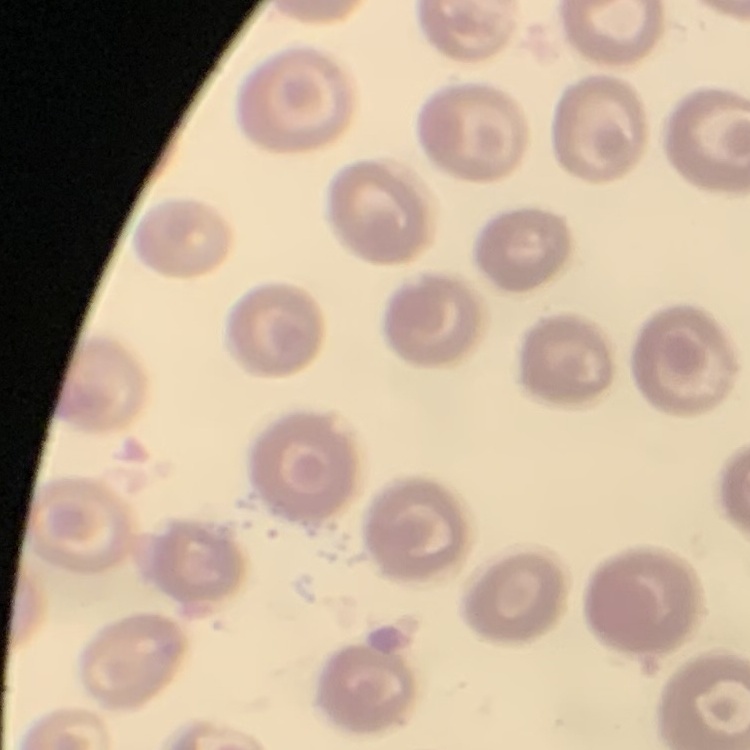
The red blood cells show no rouleaux formation. One tile cut from a larger photomicrograph. Thin blood smear. Field's or Giemsa stain.